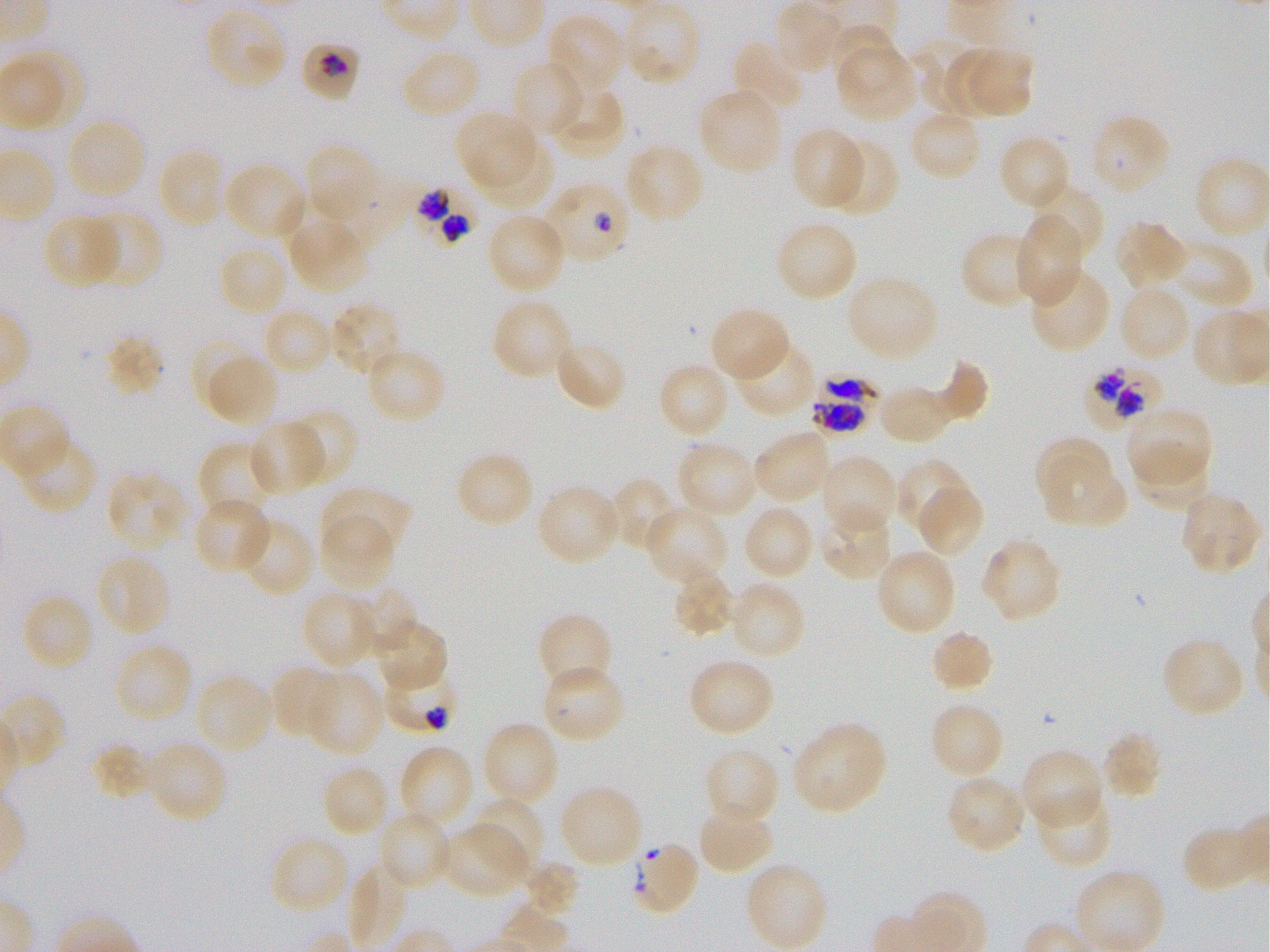

Not every red blood cell is marked. A life-cycle stage — or a range of stages, where the recorded stages span more than one — follows each staged infected red blood cell.
locations of uninfected red blood cells = approximate bounding boxes as [x1, y1, x2, y2] in pixels: [203, 4, 289, 91], [545, 12, 628, 97], [831, 24, 904, 97], [912, 38, 983, 115], [731, 39, 808, 116], [399, 47, 483, 121], [839, 48, 919, 122], [943, 48, 1010, 115], [969, 49, 1034, 118], [511, 58, 586, 141], [547, 83, 626, 158], [697, 87, 784, 177], [907, 108, 984, 182], [454, 109, 534, 183], [1088, 113, 1172, 196], [64, 117, 148, 202], [790, 127, 868, 210], [997, 133, 1073, 212], [821, 136, 899, 216], [481, 139, 557, 211], [303, 141, 381, 226], [624, 143, 706, 225], [155, 146, 227, 229], [222, 160, 310, 242], [1026, 182, 1105, 264], [80, 208, 163, 289], [41, 212, 123, 288], [485, 212, 569, 297], [1013, 217, 1083, 306], [774, 218, 859, 303], [1114, 218, 1193, 290], [290, 220, 369, 294], [961, 231, 1046, 309], [1166, 240, 1256, 311], [217, 242, 289, 318], [1028, 264, 1111, 354], [844, 273, 939, 362], [1116, 283, 1193, 364], [490, 296, 574, 381], [328, 300, 405, 378], [708, 305, 792, 383], [263, 306, 335, 377], [104, 334, 165, 397], [731, 336, 818, 419], [553, 337, 628, 412], [364, 345, 447, 424], [198, 350, 280, 428], [936, 357, 991, 421], [657, 361, 733, 440], [878, 384, 945, 444], [1123, 406, 1213, 492], [283, 409, 359, 488], [247, 419, 327, 496], [751, 428, 834, 505], [13, 432, 98, 515], [1033, 435, 1111, 497], [677, 439, 758, 519], [198, 441, 280, 523], [454, 450, 534, 529], [817, 454, 900, 538], [1043, 456, 1128, 523], [1130, 456, 1211, 508], [895, 457, 975, 541], [106, 471, 191, 554], [606, 477, 682, 554], [535, 483, 624, 567], [915, 484, 987, 560], [319, 485, 413, 561], [1178, 490, 1262, 575], [193, 496, 273, 575], [643, 504, 730, 586], [741, 504, 816, 580], [816, 504, 896, 582], [319, 515, 396, 592], [237, 516, 316, 598], [978, 536, 1063, 624], [874, 547, 957, 637], [94, 551, 172, 639], [670, 566, 737, 638], [727, 580, 807, 661], [349, 586, 419, 657], [300, 589, 381, 670], [20, 592, 96, 673], [535, 611, 612, 695], [374, 617, 448, 691], [928, 627, 995, 693], [1160, 636, 1246, 719], [113, 641, 193, 725], [686, 656, 775, 738], [540, 664, 628, 745], [269, 665, 347, 742], [303, 668, 384, 757], [193, 673, 276, 756], [928, 701, 1006, 781], [481, 720, 560, 810], [790, 720, 889, 815], [1101, 730, 1164, 800], [142, 739, 229, 824], [398, 742, 476, 830], [92, 743, 158, 802], [702, 745, 781, 827], [1019, 748, 1104, 831], [320, 762, 392, 838], [945, 774, 1028, 856], [556, 783, 644, 870], [1032, 786, 1113, 869], [470, 795, 544, 874], [695, 802, 775, 875], [375, 809, 451, 890], [438, 822, 529, 899], [1181, 823, 1268, 894], [268, 833, 351, 915], [629, 839, 700, 916], [520, 862, 578, 919], [748, 864, 828, 948]
culture = P. falciparum strain 3D7, static, in vitro
locations of infected red blood cells = approximate bounding boxes as [x1, y1, x2, y2] in pixels: [300, 42, 364, 102] trophozoite; [539, 180, 632, 265]; [410, 181, 483, 254]; [1088, 366, 1161, 428]; [813, 373, 879, 434]
donor blood group = O+
preparation = thin blood smear
image size = 1270×952 pixels
stain = Giemsa
field of view = one from this slide
locations of red blood cells of indeterminate infection status = approximate bounding boxes as [x1, y1, x2, y2] in pixels: [385, 663, 454, 730]
objective = 100x, oil immersion, numerical aperture 1.25